State which parasite is depicted.
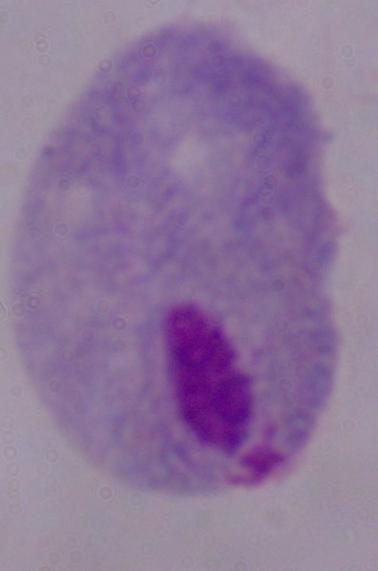
This is a trichomonad.

1000x magnification. Photomicrograph.